Report the malaria status of this cell.
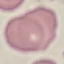

Uninfected.

Photographed with a smartphone camera at the microscope eyepiece. Cell patch, automatically extracted from a larger field of view and resized to 64 × 64 pixels. Thin blood film. Giemsa stain.